Classify this cell by malaria status.
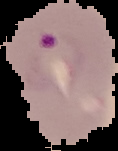

It is parasitized.

preparation = thin blood film
image size = 118×151 pixels
image type = cell region segmented out of the field of view; surrounding area masked to black